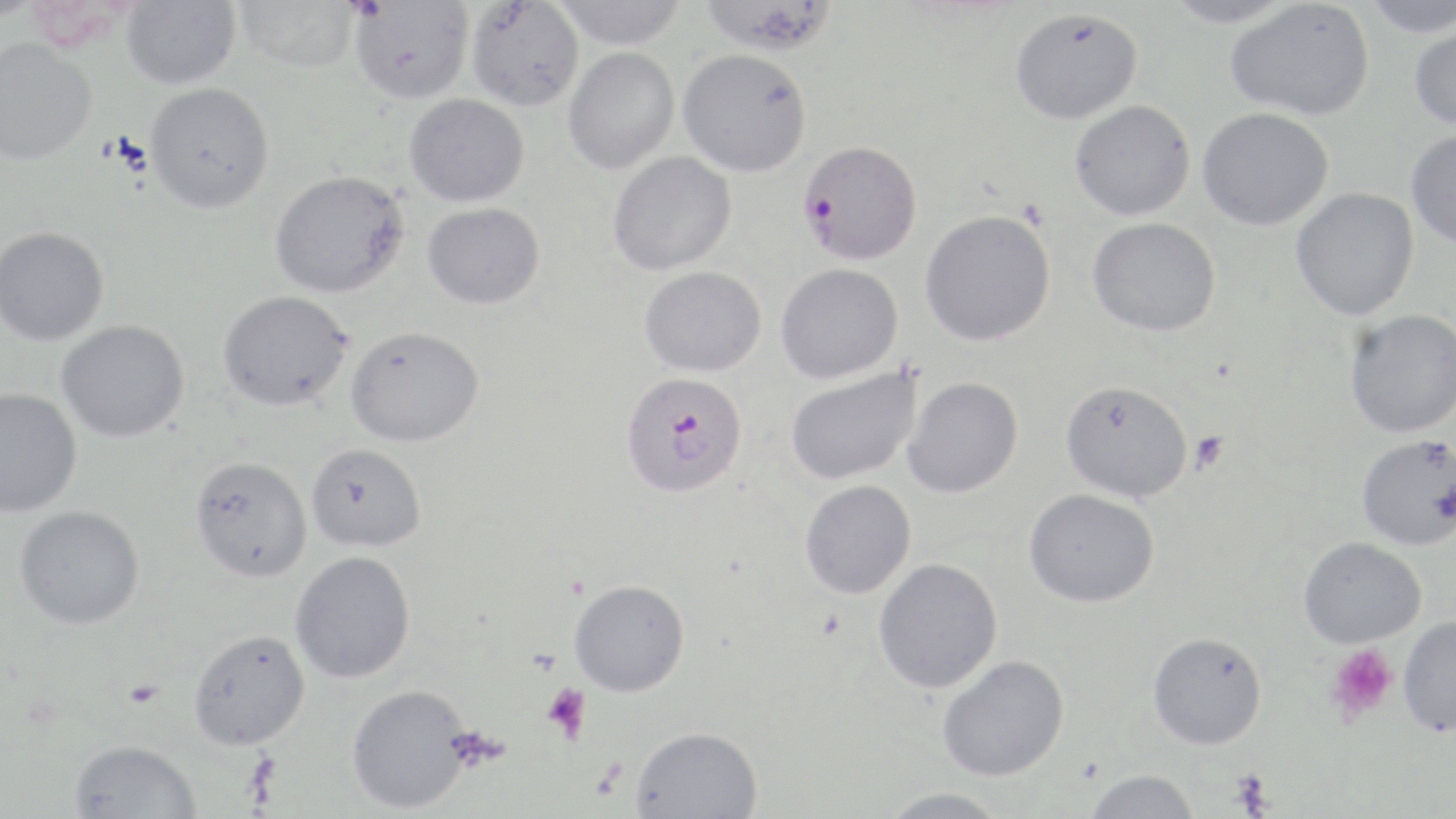

Approximate bounding boxes as [x1, y1, x2, y2] in pixels. Platelet locations: [1190, 431, 1229, 471], [1327, 644, 1399, 722], [125, 680, 164, 708], [541, 684, 591, 744], [1229, 769, 1276, 816]. Uninfected red blood cell locations: [121, 0, 241, 90], [234, 0, 360, 74], [349, 0, 474, 105], [549, 0, 689, 51], [699, 0, 838, 57], [1162, 0, 1301, 28], [1361, 0, 1456, 37], [466, 1, 584, 112], [1224, 1, 1373, 121], [1009, 8, 1143, 124], [1408, 21, 1456, 132], [0, 38, 96, 168], [564, 48, 680, 174], [678, 51, 812, 178], [144, 83, 274, 213], [405, 94, 529, 207], [1069, 100, 1195, 221], [1196, 107, 1334, 231], [1406, 129, 1456, 249], [607, 151, 737, 276], [269, 170, 409, 298], [1290, 187, 1419, 321], [422, 202, 545, 310], [920, 209, 1056, 346], [1087, 217, 1221, 337], [0, 226, 109, 345], [776, 263, 903, 385], [639, 266, 766, 377], [217, 290, 352, 411], [1344, 309, 1456, 438], [56, 320, 189, 442], [345, 325, 484, 447], [785, 366, 923, 486], [902, 376, 1024, 498], [1060, 380, 1193, 502], [0, 388, 82, 517], [1356, 434, 1456, 551], [306, 443, 426, 552], [189, 456, 312, 582], [800, 480, 917, 599], [1024, 488, 1159, 607], [14, 506, 144, 630], [1298, 537, 1426, 648], [289, 551, 415, 683], [873, 558, 1003, 693], [569, 579, 690, 697], [1398, 616, 1456, 737], [188, 628, 310, 749], [1148, 631, 1267, 750], [937, 655, 1069, 781], [346, 684, 472, 814], [630, 726, 762, 818], [69, 739, 203, 819], [1084, 769, 1200, 818], [878, 787, 1010, 819]. Plasmodium falciparum-infected red blood cell locations: [798, 141, 922, 266], [621, 372, 748, 499]. Slide-level diagnosis: Plasmodium falciparum. May-Grünwald-Giemsa stain. One field of a larger specimen. Thin blood film. Optical microscopy. Image is 1456×819 pixels. 1000x magnification.